Identify the cell.
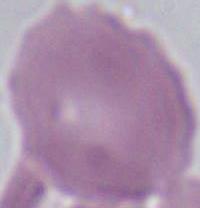

An erythrocyte.

Captured at 1000x magnification. Micrograph.